State which cell type is depicted.
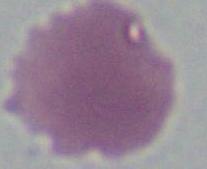
This is an erythrocyte.

Summary:
  - Modality: photomicrograph
  - Magnification: 1000x